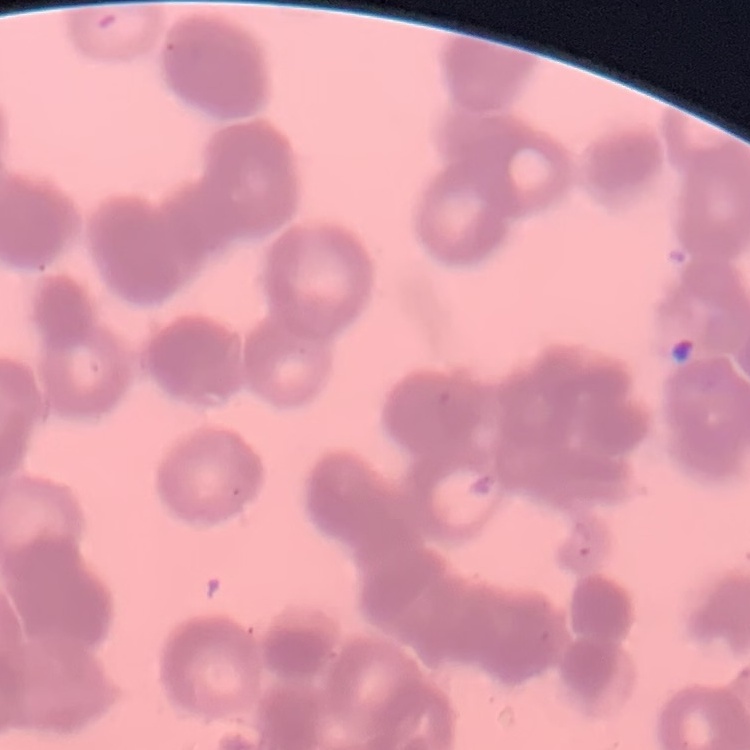
erythrocyte morphology = rouleaux formation
stain = Field's or Giemsa
preparation = thin blood smear
image type = one tile cut from a larger photomicrograph